Comment on the morphology of the red blood cells.
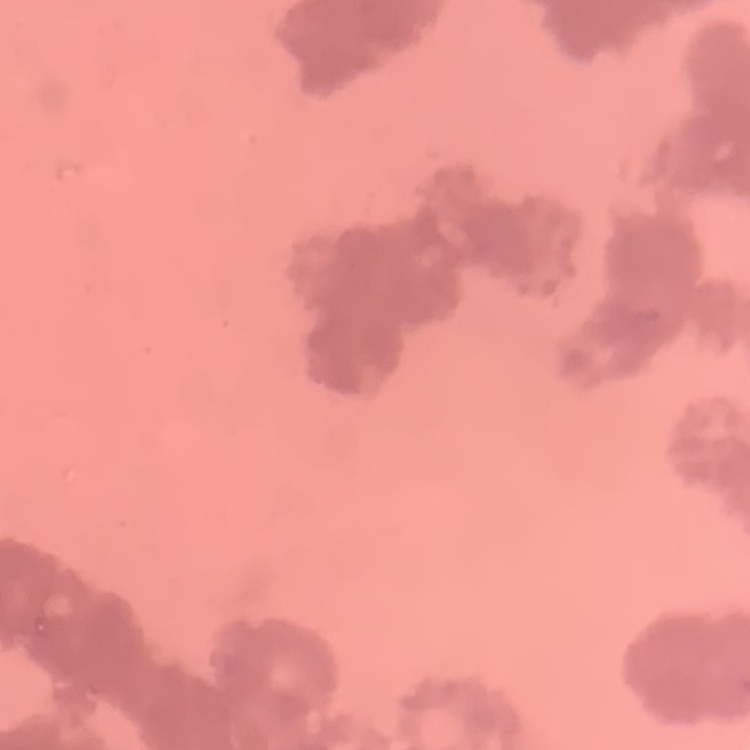

Rouleaux formation.

Field's or Giemsa stain. Square crop of a larger photomicrograph. Thin blood film.